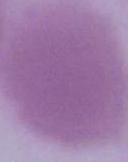

Summary:
  - Modality: photomicrograph
  - Magnification: 1000x
  - Identification: erythrocyte